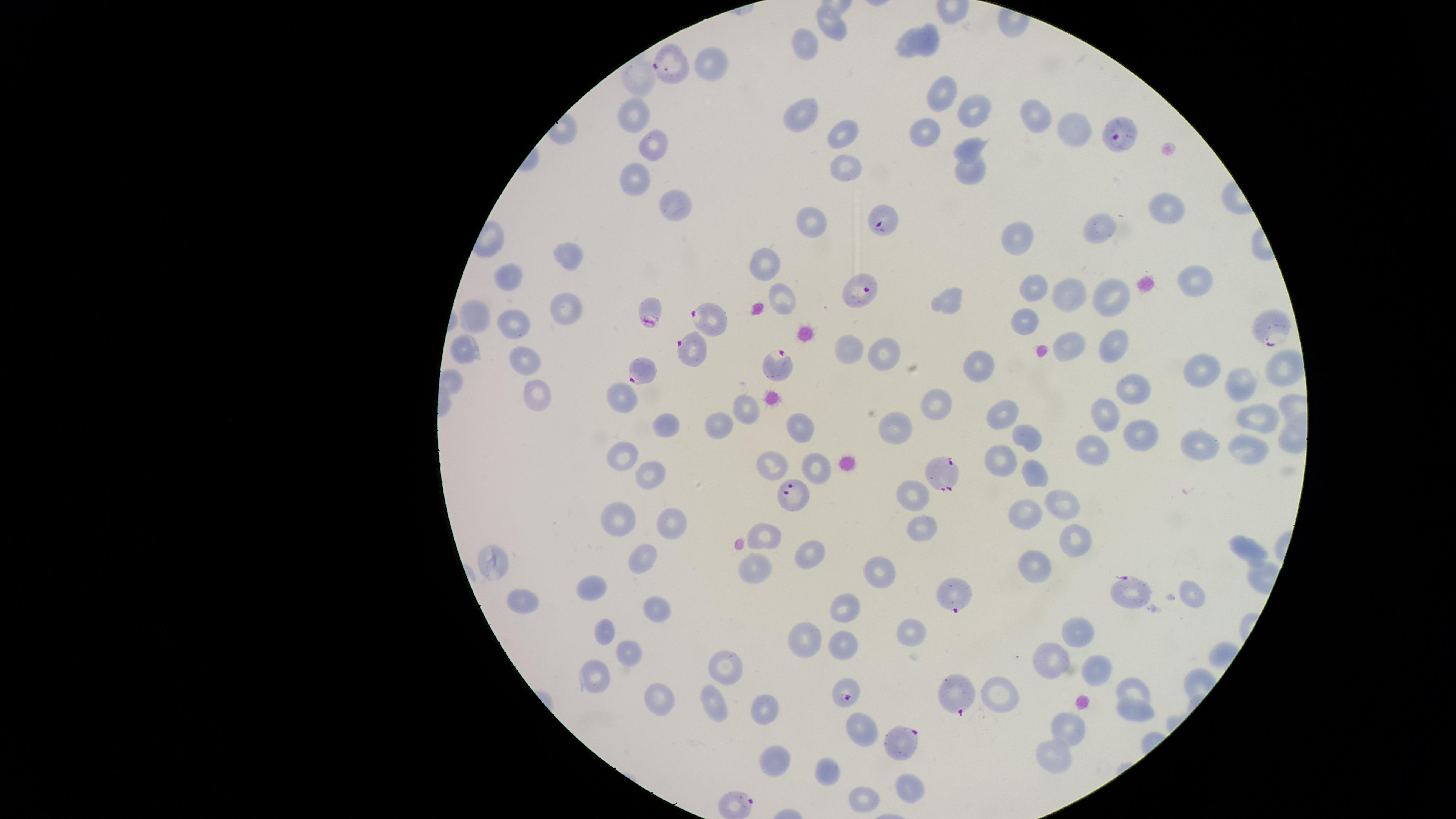

image size = 1456×819 pixels
uninfected RBCs = approximate marker points as (x, y) in pixels: (830, 23), (931, 32), (803, 46), (905, 46), (713, 69), (635, 80), (944, 92), (975, 106), (1033, 112), (634, 114), (803, 115), (1070, 127), (925, 131), (847, 135), (655, 143), (971, 145), (845, 168), (974, 170), (634, 176), (670, 200), (1164, 208), (814, 220), (1097, 228), (1018, 238), (567, 254), (761, 261), (1200, 278), (512, 279), (1035, 286), (1110, 294), (1069, 295), (786, 297), (947, 299), (567, 305), (479, 314), (1025, 319), (510, 325), (1111, 343), (1070, 346), (467, 350), (847, 350), (886, 353), (524, 357), (978, 362), (1285, 366), (1201, 367), (1238, 380), (1137, 388), (535, 390), (623, 393), (938, 404), (743, 412), (1003, 413), (1103, 413), (1260, 420), (665, 423), (714, 424), (800, 428), (900, 432), (1139, 433), (1025, 436), (1198, 443), (1244, 448), (621, 453), (1090, 453), (998, 455), (775, 465), (813, 467), (648, 472), (1038, 472), (910, 490), (1060, 498), (1025, 512), (614, 514), (670, 524), (923, 530), (767, 532), (1070, 536), (1250, 548), (811, 555), (641, 558), (1035, 561), (494, 565), (882, 568), (752, 570), (591, 582), (1193, 592), (847, 601), (525, 602), (654, 605), (911, 628), (604, 629), (810, 629), (1082, 634), (837, 642), (628, 655), (1057, 656), (724, 666), (1095, 672), (597, 681), (1139, 688), (998, 692), (649, 697), (714, 702), (762, 709), (1134, 713), (861, 725), (1068, 729), (1050, 757), (777, 762), (831, 763), (910, 783), (860, 798)
presence = malaria parasites identified
preparation = thin smear of blood
visible region = circular
stain = Giemsa
capture = smartphone photograph through the microscope eyepiece
field of view = single
species = Plasmodium falciparum
parasitized RBCs = approximate marker points as (x, y) in pixels: (669, 64), (1117, 134), (885, 220), (863, 290), (710, 314), (1269, 324), (696, 344), (778, 364), (641, 368), (940, 470), (792, 496), (1128, 590), (955, 595), (845, 692), (960, 692), (904, 739)